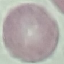
malaria status = uninfected
capture = smartphone camera at the microscope eyepiece
preparation = thin blood smear
image type = cell patch, automatically extracted from a larger field of view and resized to 64 × 64 pixels
stain = Giemsa